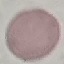 Malaria status: uninfected. Automatically extracted cell patch, resized to 64 × 64 pixels. Photographed with a smartphone camera at the microscope eyepiece. Giemsa stain. Thin blood film.